Report the malaria status of this cell.
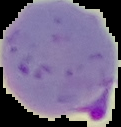

Parasitized.

image size = 121×127 pixels
image type = segmented cell region on a black background
preparation = thin blood smear